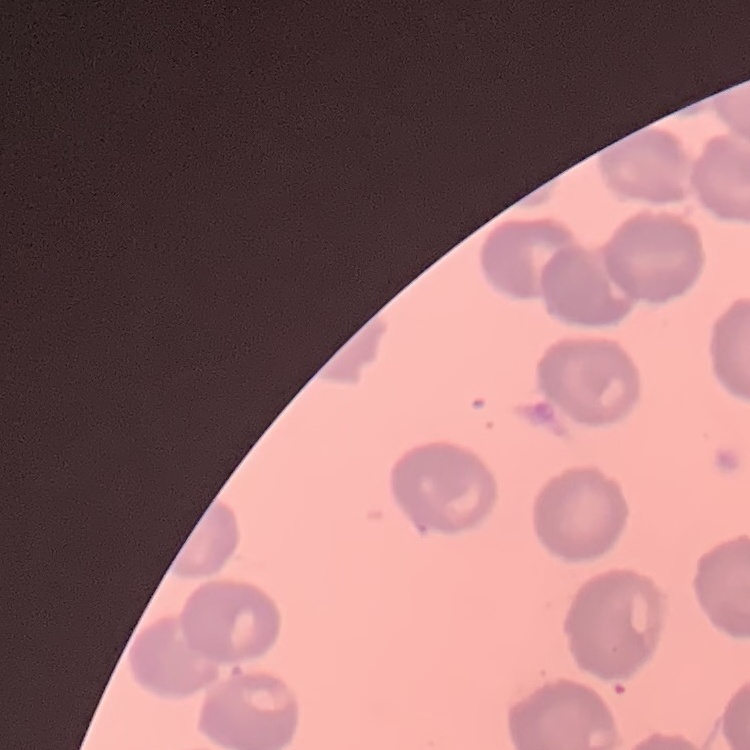

The erythrocytes show no rouleaux formation. Thin blood smear. Field's or Giemsa stain. One tile cut from a larger photomicrograph.